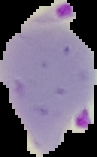

Summary:
  - Image type: segmented cell region with the area outside set to black
  - Preparation: thin blood film
  - Malaria status: parasitized
  - Image size: 97×157 pixels